Assess this cell for malaria.
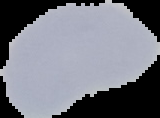

Uninfected.

{
  "preparation": "thin blood smear",
  "image_size": "160×118 pixels",
  "image_type": "cell region segmented out of the field of view; surrounding area masked to black"
}